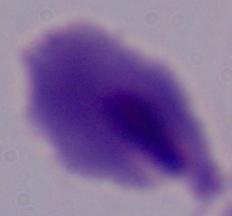

Summary:
  - Modality: photomicrograph
  - Identification: trichomonad
  - Magnification: 1000x